Assess the morphology of the red blood cells.
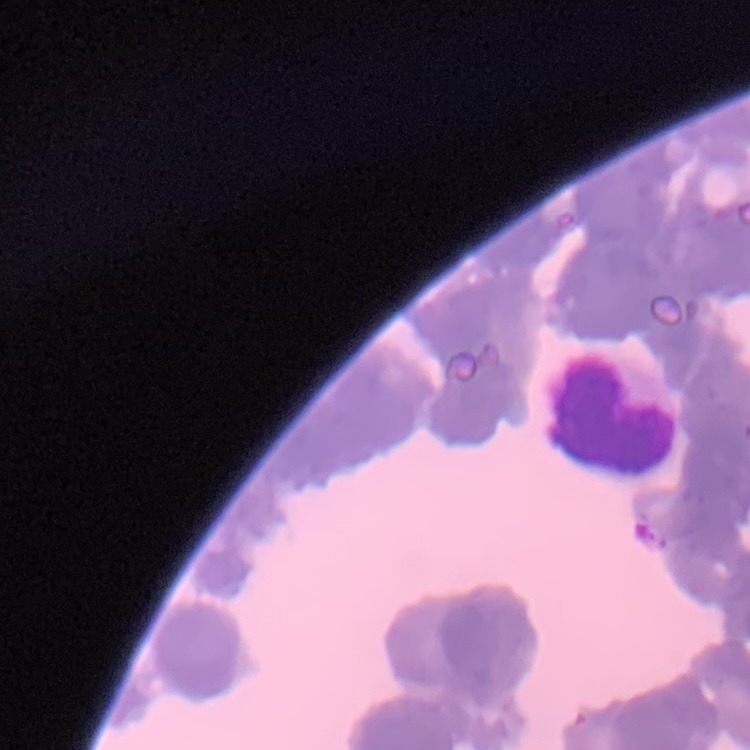

They show rouleaux formation.

{
  "stain": "Field's or Giemsa",
  "image_type": "one tile cut from a larger photomicrograph",
  "preparation": "thin peripheral smear"
}